Give the position of every malaria parasite and every leukocyte.
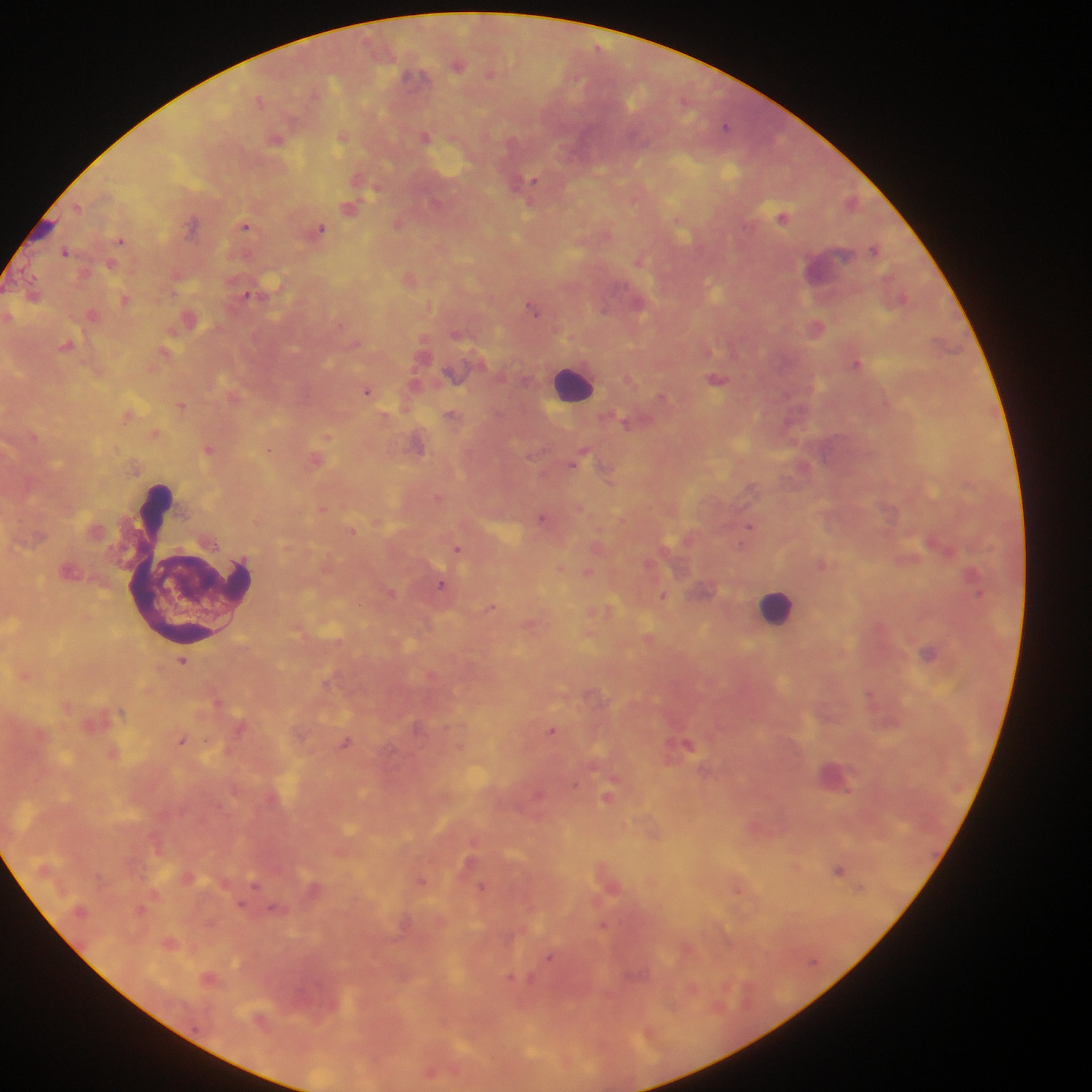
Approximate centers as (x, y) in pixels.
Malaria parasites (some below the resolvable threshold): (598, 49), (725, 126), (535, 181), (78, 206), (193, 224), (245, 226), (320, 228), (120, 240), (876, 249), (65, 252), (247, 294), (534, 307), (856, 362), (367, 391), (269, 450), (541, 516), (751, 526), (742, 542), (458, 548), (442, 583), (663, 595), (492, 607), (553, 730), (183, 741), (576, 784), (848, 790), (423, 880), (255, 888), (481, 889), (240, 903), (603, 924), (550, 958), (512, 978).
Leukocytes: (577, 383), (194, 567), (775, 605).

Summary:
  - Field of view: single
  - Image size: 1092×1092 pixels
  - Preparation: thick blood film
  - Capture: mobile-phone photograph through a microscope
  - Country: Ghana